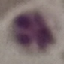
Result: no malaria parasites detected. Thin smear of blood. Giemsa-stained preparation. Automatically extracted cell patch, resized to 64 × 64 pixels. Photographed with a smartphone camera at the microscope eyepiece.